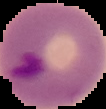
Malaria status: parasitized. Image is 106×109 pixels. Cell region segmented out of the field of view; the surrounding area is masked to black. From a thin blood smear.